Assess the morphology of the erythrocytes.
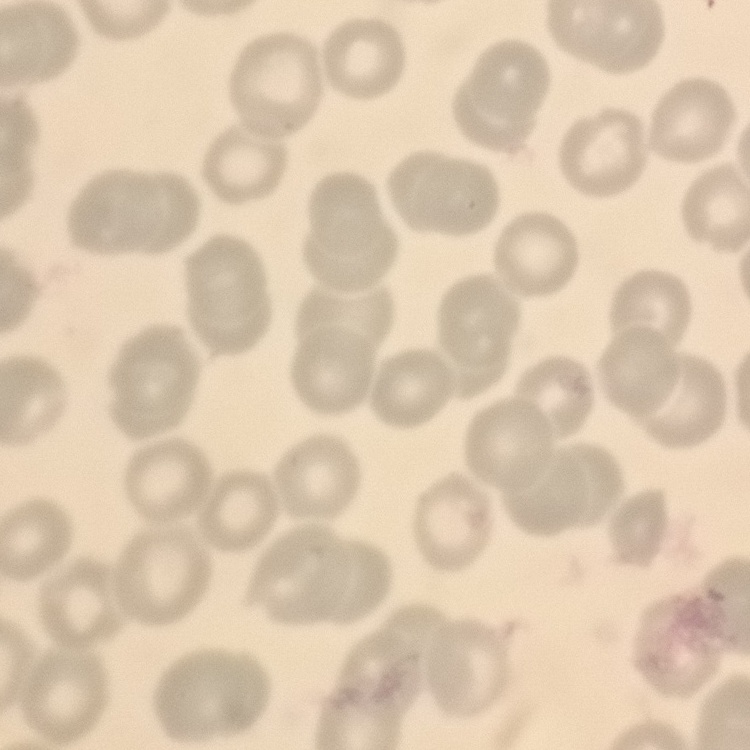
No rouleaux formation.

One tile cut from a larger photomicrograph. Thin blood smear. Field's or Giemsa stain.